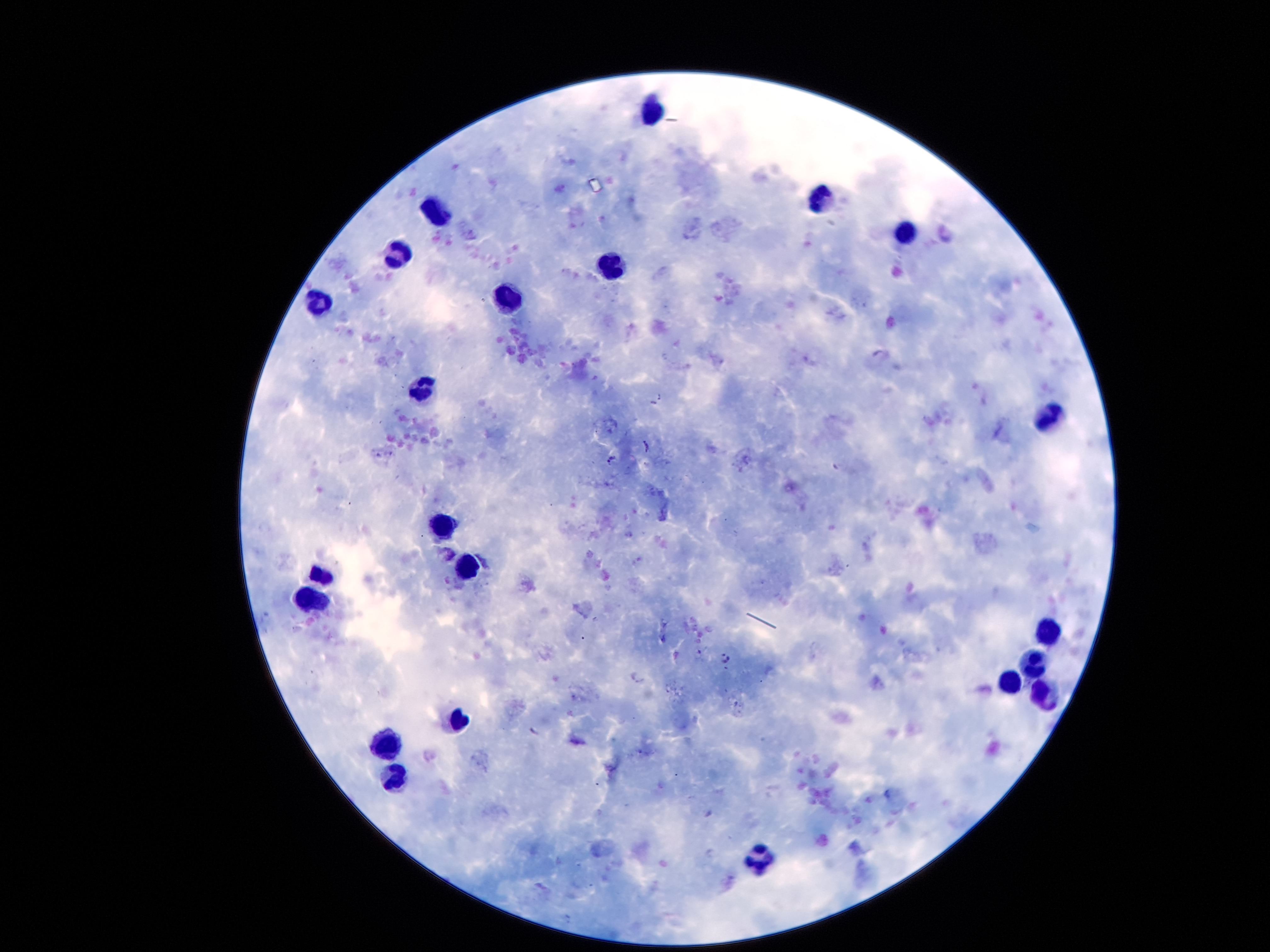
coordinate format = approximate object centers, in pixels from the top-left corner
leukocyte locations = (x=652, y=112), (x=820, y=200), (x=438, y=211), (x=906, y=235), (x=398, y=256), (x=610, y=268), (x=316, y=304), (x=506, y=309), (x=424, y=390), (x=1047, y=418), (x=440, y=527), (x=468, y=567), (x=320, y=575), (x=314, y=596), (x=1051, y=630), (x=1033, y=665), (x=1013, y=683), (x=1043, y=697), (x=460, y=721), (x=386, y=743), (x=398, y=773), (x=762, y=855)
Plasmodium parasite locations = (x=880, y=354), (x=660, y=395), (x=653, y=404), (x=647, y=446), (x=610, y=459), (x=724, y=659), (x=636, y=676), (x=535, y=732)
patient malaria status = infected with Plasmodium falciparum
stain = Giemsa
magnification = 100x
field of view = one from this slide
preparation = thick blood smear
capture = smartphone camera through the microscope eyepiece
image size = 1270×952 pixels